Identify the parasite.
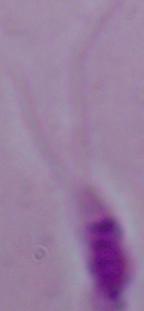
This is Leishmania.

Summary:
  - Magnification: 1000x
  - Modality: photomicrograph